Classify this cell by malaria status.
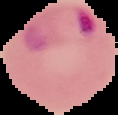

Parasitized.

image size = 118×115 pixels
preparation = thin blood film
image type = segmented cell region on a black background